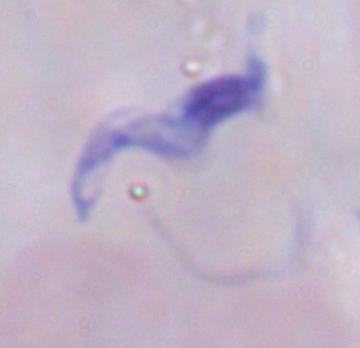
Summary:
  - Magnification: 1000x
  - Modality: micrograph
  - Identification: trypanosome